Classify this cell by malaria status.
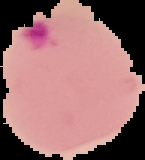

It is parasitized.

Segmented cell region on a black background. Image is 145×160 pixels. From a thin blood film.